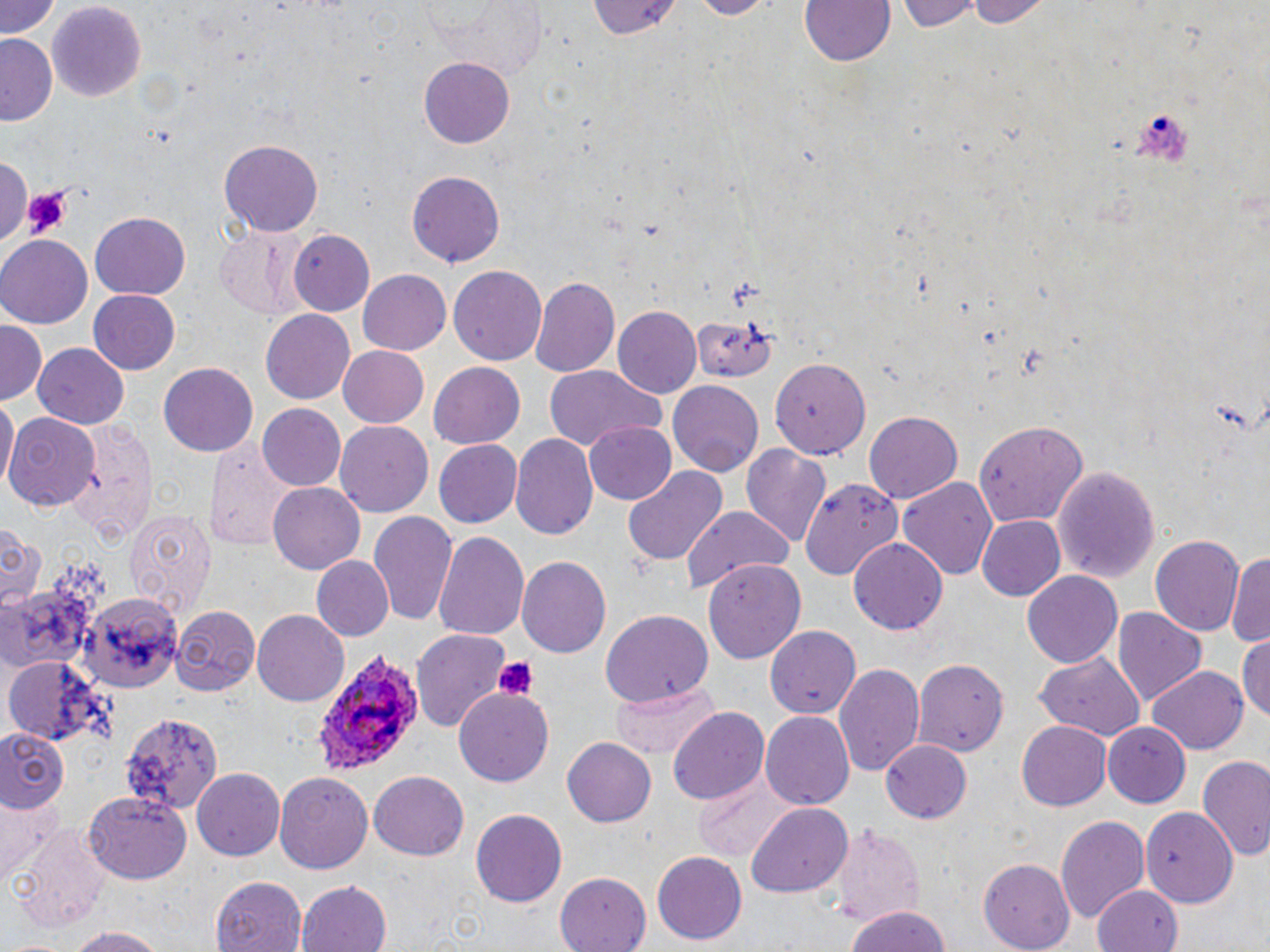

Plasmodium ovale-infected red blood cell locations = approximate bounding boxes as (x1,y1)-(x2,y2) corner pairs in pixels: (312,649)-(421,774)
slide-level diagnosis = Plasmodium ovale
stain = May-Grünwald-Giemsa
uninfected red blood cell locations = approximate bounding boxes as (x1,y1)-(x2,y2) corner pairs in pixels: (2,0)-(61,43), (685,0)-(779,19), (800,0)-(895,69), (899,0)-(982,31), (964,0)-(1051,28), (423,1)-(550,72), (584,1)-(681,44), (45,2)-(148,103), (2,35)-(60,126), (420,46)-(511,242), (420,57)-(514,147), (220,140)-(324,236), (0,157)-(27,245), (407,170)-(505,267), (90,212)-(189,299), (216,222)-(310,319), (289,229)-(376,316), (0,236)-(93,329), (448,265)-(547,365), (357,269)-(451,356), (530,276)-(619,375), (88,289)-(181,375), (693,302)-(783,386), (614,305)-(702,397), (261,310)-(355,405), (0,321)-(45,405), (34,341)-(130,429), (337,345)-(430,428), (770,356)-(872,460), (428,361)-(526,449), (159,363)-(258,456), (543,364)-(666,453), (669,382)-(762,473), (1,394)-(17,493), (257,404)-(347,492), (864,409)-(963,502), (5,411)-(101,509), (70,418)-(161,539), (335,420)-(433,518), (583,420)-(677,505), (976,422)-(1090,527), (511,432)-(598,541), (206,438)-(299,550), (435,440)-(523,528), (740,442)-(833,550), (1051,463)-(1160,584), (622,467)-(726,569), (896,475)-(1000,582), (799,477)-(904,579), (267,482)-(367,575), (681,506)-(794,592), (124,509)-(216,622), (370,510)-(458,627), (977,515)-(1067,602), (0,525)-(43,612), (433,528)-(530,643), (1150,533)-(1245,638), (849,536)-(947,632), (1228,550)-(1269,654), (312,556)-(394,641), (517,556)-(610,658), (702,561)-(804,661), (1023,569)-(1122,665), (0,581)-(95,668), (76,589)-(181,692), (171,604)-(259,693), (253,609)-(350,705), (600,610)-(712,703), (1114,611)-(1205,706), (766,623)-(863,718), (412,631)-(510,730), (1235,636)-(1270,722), (1033,652)-(1146,743), (914,659)-(1008,756), (5,661)-(101,745), (834,662)-(925,777), (1147,666)-(1248,756), (610,682)-(720,763), (455,689)-(554,785), (669,707)-(768,807), (117,711)-(220,812), (761,711)-(854,810), (1017,721)-(1112,811), (1104,723)-(1191,807), (0,729)-(69,811), (563,737)-(655,828), (881,740)-(972,825), (1200,755)-(1270,863), (193,767)-(287,861), (368,770)-(469,860), (275,772)-(373,875), (690,775)-(797,861), (84,793)-(189,886), (0,796)-(64,881), (747,802)-(852,898), (1140,802)-(1239,910), (471,809)-(566,907), (1056,814)-(1151,927), (832,825)-(925,924), (652,851)-(747,945), (979,857)-(1074,949), (555,870)-(654,952), (210,871)-(308,950), (295,880)-(394,952), (1090,883)-(1184,952), (844,905)-(954,952), (63,925)-(169,952)
preparation = thin blood smear
field of view = one of a larger specimen
platelet locations = approximate bounding boxes as (x1,y1)-(x2,y2) corner pairs in pixels: (1133,110)-(1189,165), (18,183)-(71,236), (493,657)-(537,700)
modality = light microscopy
image size = 1270×952 pixels
magnification = 1000x